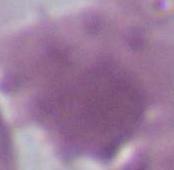
identification: erythrocyte
modality: photomicrograph
magnification: 1000x